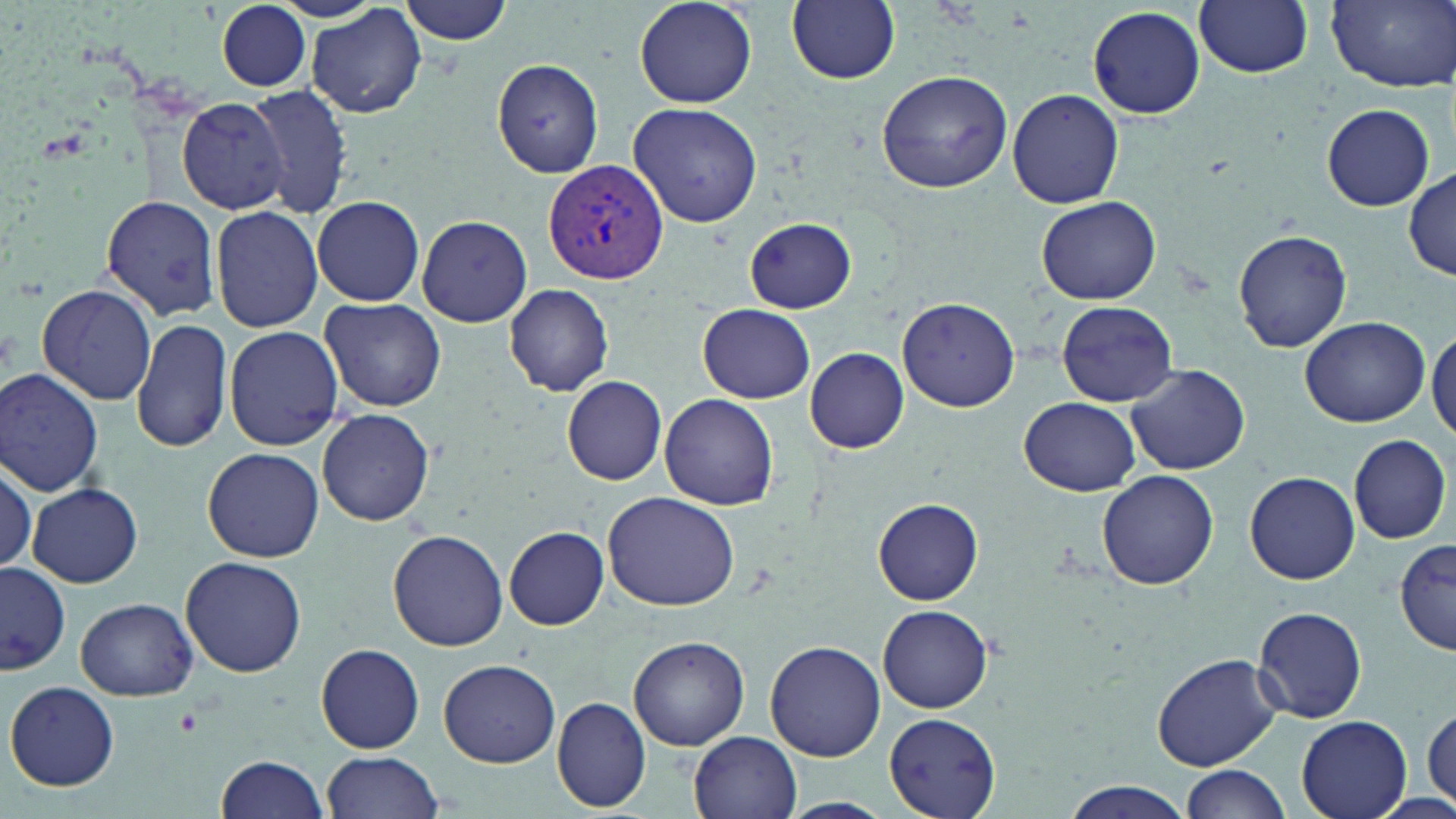

Plasmodium vivax-infected red blood cell locations = approximate bounding boxes as [x1, y1, x2, y2] in pixels: [544, 158, 668, 284]
slide-level diagnosis = Plasmodium vivax
preparation = thin blood smear
field of view = one of a larger specimen
modality = light microscopy
uninfected red blood cell locations = approximate bounding boxes as [x1, y1, x2, y2] in pixels: [399, 0, 514, 45], [631, 0, 759, 110], [786, 0, 900, 86], [1195, 0, 1315, 79], [1325, 0, 1455, 91], [212, 1, 315, 93], [306, 4, 428, 119], [1086, 6, 1206, 118], [493, 58, 606, 179], [876, 68, 1013, 194], [250, 83, 355, 218], [1007, 89, 1124, 208], [176, 96, 291, 214], [629, 102, 764, 228], [1321, 103, 1436, 211], [1406, 166, 1456, 281], [100, 192, 223, 322], [313, 195, 425, 307], [1036, 197, 1160, 305], [210, 206, 323, 332], [417, 215, 533, 327], [744, 219, 859, 314], [1233, 228, 1353, 353], [37, 283, 156, 406], [503, 283, 614, 396], [320, 297, 446, 413], [898, 297, 1020, 410], [1057, 301, 1176, 407], [699, 304, 816, 403], [131, 315, 229, 455], [1300, 316, 1429, 427], [223, 325, 343, 451], [1428, 326, 1456, 441], [805, 347, 909, 454], [1127, 364, 1250, 474], [1, 368, 105, 498], [562, 377, 666, 485], [660, 392, 779, 511], [1019, 396, 1140, 496], [316, 409, 435, 527], [1350, 434, 1451, 544], [202, 447, 325, 562], [0, 459, 36, 582], [1096, 469, 1219, 592], [1244, 470, 1360, 585], [25, 482, 143, 587], [604, 491, 740, 609], [873, 499, 984, 604], [504, 526, 609, 630], [387, 530, 508, 651], [1396, 538, 1455, 655], [182, 557, 306, 678], [0, 562, 70, 673], [76, 597, 198, 699], [877, 604, 996, 713], [1251, 608, 1369, 722], [628, 635, 749, 751], [765, 641, 885, 762], [315, 644, 425, 753], [1151, 652, 1282, 770], [439, 658, 561, 767], [5, 681, 120, 791], [553, 696, 652, 812], [1423, 703, 1456, 809], [883, 711, 1001, 819], [1296, 715, 1413, 819], [690, 731, 802, 818], [319, 751, 443, 818], [215, 753, 332, 819], [1180, 764, 1293, 819], [1059, 783, 1197, 818], [776, 798, 895, 818]
magnification = 1000x
image size = 1456×819 pixels
stain = May-Grünwald-Giemsa